Locate every leukocyte (white blood cell).
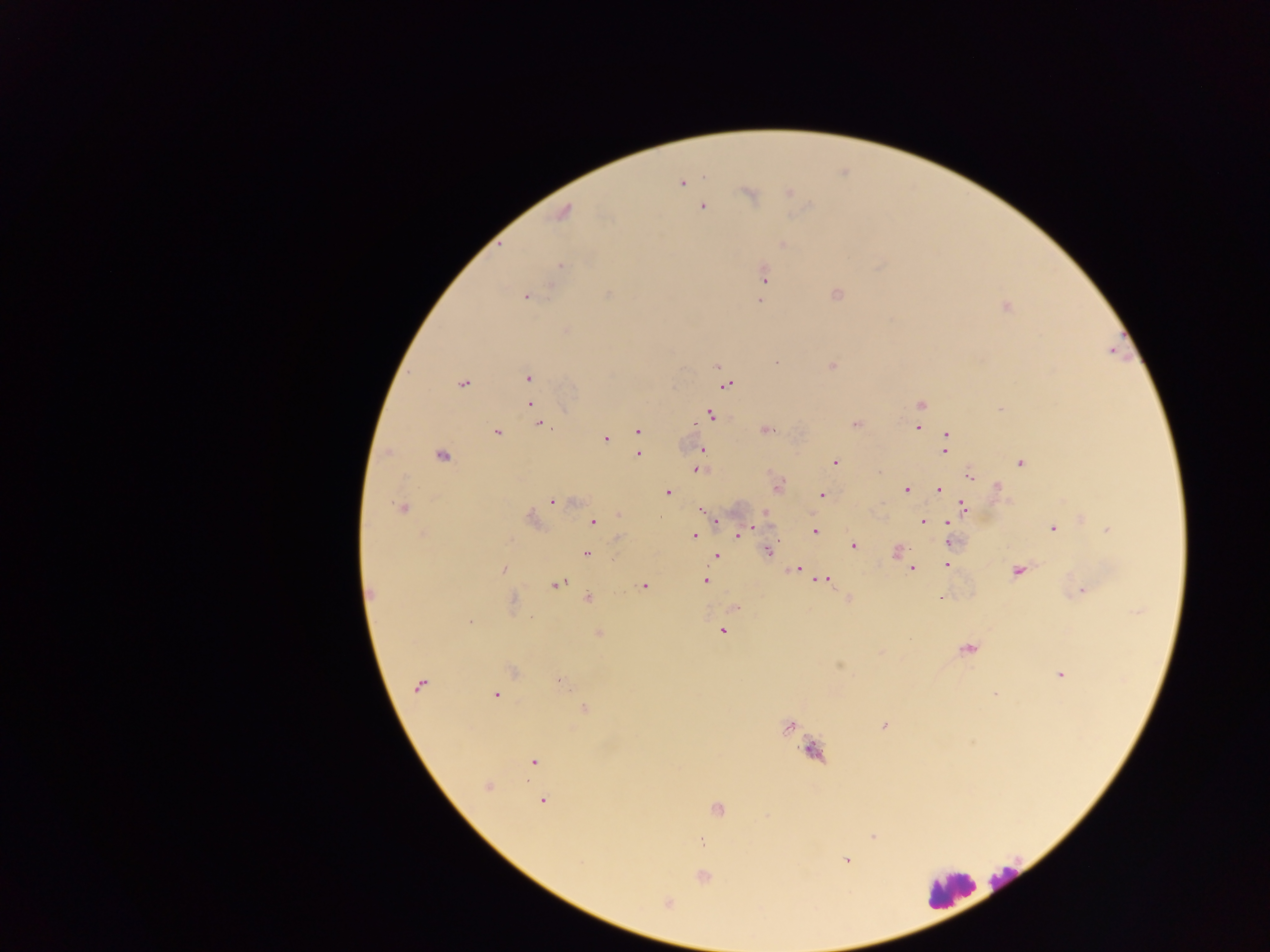
Approximate centers as [x, y] in pixels.
Leukocytes: [1005, 883], [949, 890].

Summary:
  - Plasmodium parasite locations: [681, 183], [788, 192], [749, 194], [702, 207], [563, 212], [782, 245], [560, 266], [764, 275], [608, 294], [837, 294], [526, 296], [759, 301], [1005, 307], [776, 362], [717, 366], [831, 366], [528, 378], [463, 384], [726, 386], [531, 405], [921, 405], [1000, 408], [711, 416], [539, 423], [856, 424], [917, 428], [766, 430], [638, 431], [496, 432], [947, 434], [605, 439], [944, 449], [701, 450], [638, 454], [441, 456], [835, 462], [1021, 463], [697, 469], [878, 473], [969, 476], [779, 486], [996, 486], [938, 489], [907, 490], [667, 492], [822, 495], [553, 501], [963, 506], [402, 509], [702, 509], [765, 514], [619, 515], [1082, 518], [532, 520], [716, 520], [593, 522], [923, 522], [950, 522], [1052, 529], [1108, 530], [746, 531], [815, 531], [739, 533], [694, 536], [950, 542], [853, 545], [768, 550], [897, 551], [587, 553], [716, 556], [908, 563], [946, 564], [912, 569], [503, 570], [797, 570], [1018, 571], [705, 580], [826, 580], [556, 585], [644, 586], [1083, 590], [371, 592], [589, 598], [940, 598], [735, 608], [470, 621], [722, 631], [599, 633], [967, 649], [881, 653], [839, 666], [513, 672], [1061, 675], [560, 682], [419, 685], [995, 694], [495, 695], [584, 709], [884, 725], [789, 726], [813, 751], [533, 762], [487, 786], [542, 801], [717, 810], [873, 837], [846, 861], [703, 877], [668, 903]
  - Image size: 1270×952 pixels
  - Preparation: thick blood smear
  - Country: Ghana
  - Field of view: single
  - Capture: mobile-phone photograph through a microscope